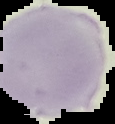
Summary:
  - Result: negative for malaria parasites
  - Preparation: thin blood smear
  - Image size: 115×124 pixels
  - Image type: segmented cell region with the area outside set to black